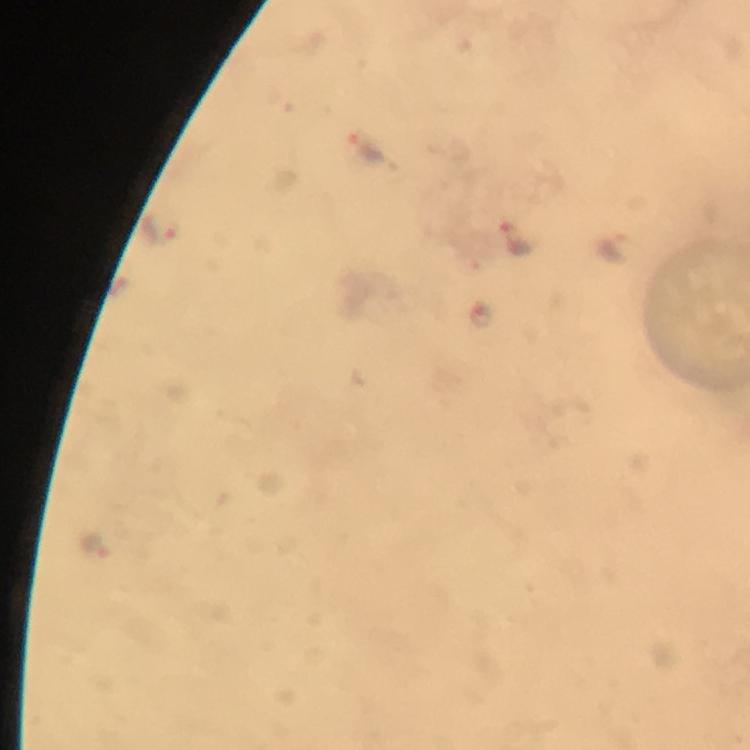

stain: Giemsa
immersion_oil: used
cropped_from: a single field of view
magnification: 100x
preparation: thick smear
image_size: 750×750 pixels
plasmodium_parasite_locations: 'approximate object centers, in pixels from the top-left corner: (x=364, y=148), (x=156, y=228), (x=518, y=239), (x=617, y=250)'
capture: smartphone camera through the microscope
context: from a malaria diagnostic workup